Locate every blood parasite and identify its species.
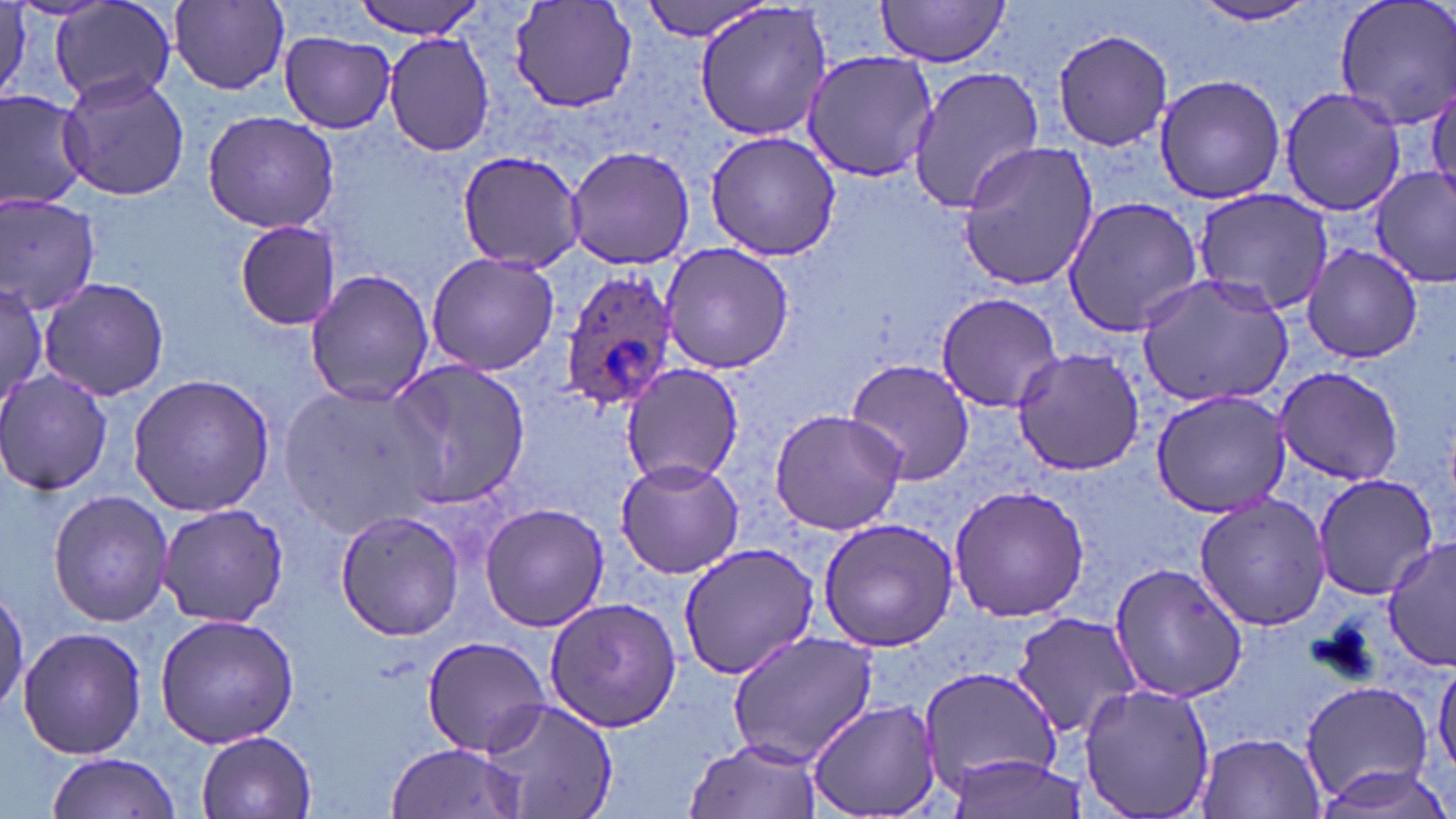

Approximate bounding boxes as (x1,y1)-(x2,y2) corner pairs in pixels.
Plasmodium ovale-infected red blood cells: (560,267)-(678,413).
No Plasmodium falciparum, Plasmodium malariae, Plasmodium vivax, Babesia divergens, or Trypanosoma brucei observed.

{
  "slide_level_diagnosis": "Plasmodium ovale",
  "stain": "May-Grünwald-Giemsa",
  "field_of_view": "one of a larger specimen",
  "image_size": "1456×819 pixels",
  "preparation": "thin blood smear",
  "modality": "light microscopy",
  "uninfected_red_blood_cell_locations": "approximate bounding boxes as (x1,y1)-(x2,y2) corner pairs in pixels: (48,0)-(178,110), (349,0)-(493,39), (640,0)-(774,41), (874,0)-(1012,68), (1188,0)-(1328,28), (1332,0)-(1456,132), (169,1)-(289,92), (510,2)-(637,114), (693,3)-(832,143), (1050,27)-(1176,152), (383,30)-(495,158), (279,33)-(396,133), (799,49)-(938,182), (907,65)-(1044,214), (58,72)-(190,202), (1155,73)-(1286,206), (1428,84)-(1456,207), (1278,86)-(1406,215), (0,89)-(89,209), (202,110)-(339,235), (703,131)-(843,261), (956,142)-(1100,294), (565,144)-(698,271), (455,149)-(588,271), (1371,168)-(1456,285), (1193,188)-(1333,317), (0,195)-(102,315), (1062,195)-(1207,337), (232,219)-(341,332), (660,242)-(796,373), (1302,244)-(1425,365), (425,251)-(560,378), (304,268)-(435,406), (1134,273)-(1295,410), (39,277)-(169,401), (0,281)-(49,413), (935,292)-(1062,413), (1012,348)-(1145,475), (844,357)-(977,486), (386,360)-(532,511), (622,362)-(747,487), (1272,364)-(1403,487), (0,371)-(112,497), (126,373)-(276,517), (280,381)-(443,536), (1150,388)-(1291,518), (768,408)-(908,536), (613,457)-(743,579), (1311,472)-(1441,601), (948,482)-(1093,624), (48,492)-(173,627), (1192,495)-(1330,632), (479,502)-(609,632), (156,505)-(290,627), (335,510)-(467,641), (816,516)-(959,653), (1382,538)-(1456,671), (678,541)-(820,681), (1107,560)-(1246,705), (0,586)-(28,710), (543,596)-(681,732), (154,611)-(300,748), (1009,612)-(1143,738), (16,625)-(148,760), (727,631)-(879,766), (422,636)-(552,754), (1432,659)-(1456,778), (920,669)-(1066,803), (1078,680)-(1216,819), (1298,680)-(1437,807), (477,698)-(618,819), (805,700)-(944,819), (196,731)-(315,819), (1197,731)-(1325,818), (385,740)-(526,818), (683,740)-(824,819), (942,752)-(1089,818), (45,753)-(188,819), (1310,756)-(1456,818)",
  "magnification": "1000x"
}